Assess the morphology of the red blood cells.
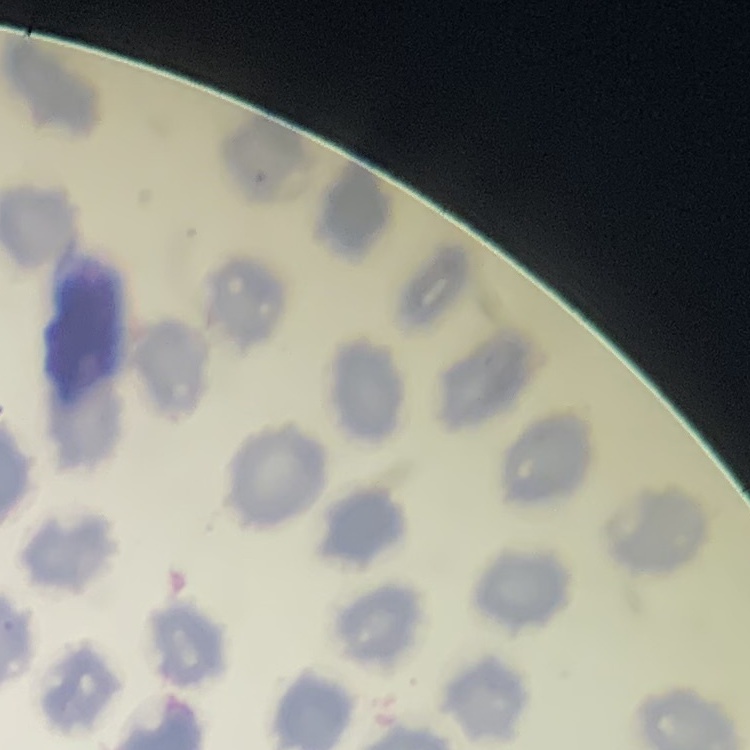
No rouleaux formation.

{
  "preparation": "thin blood smear",
  "stain": "Field's or Giemsa",
  "image_type": "one tile cut from a larger photomicrograph"
}